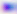

Summary:
  - Magnification: 400x
  - Identification: Toxoplasma gondii
  - Modality: photomicrograph